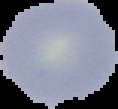

Image is 118×109 pixels. Malaria status: uninfected. From a thin blood film. Cell region segmented out of the field of view; the surrounding area is masked to black.